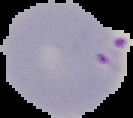
Cell region segmented out of the field of view; the surrounding area is masked to black. Image is 133×118 pixels. From a thin blood film. Result: malaria parasites identified.